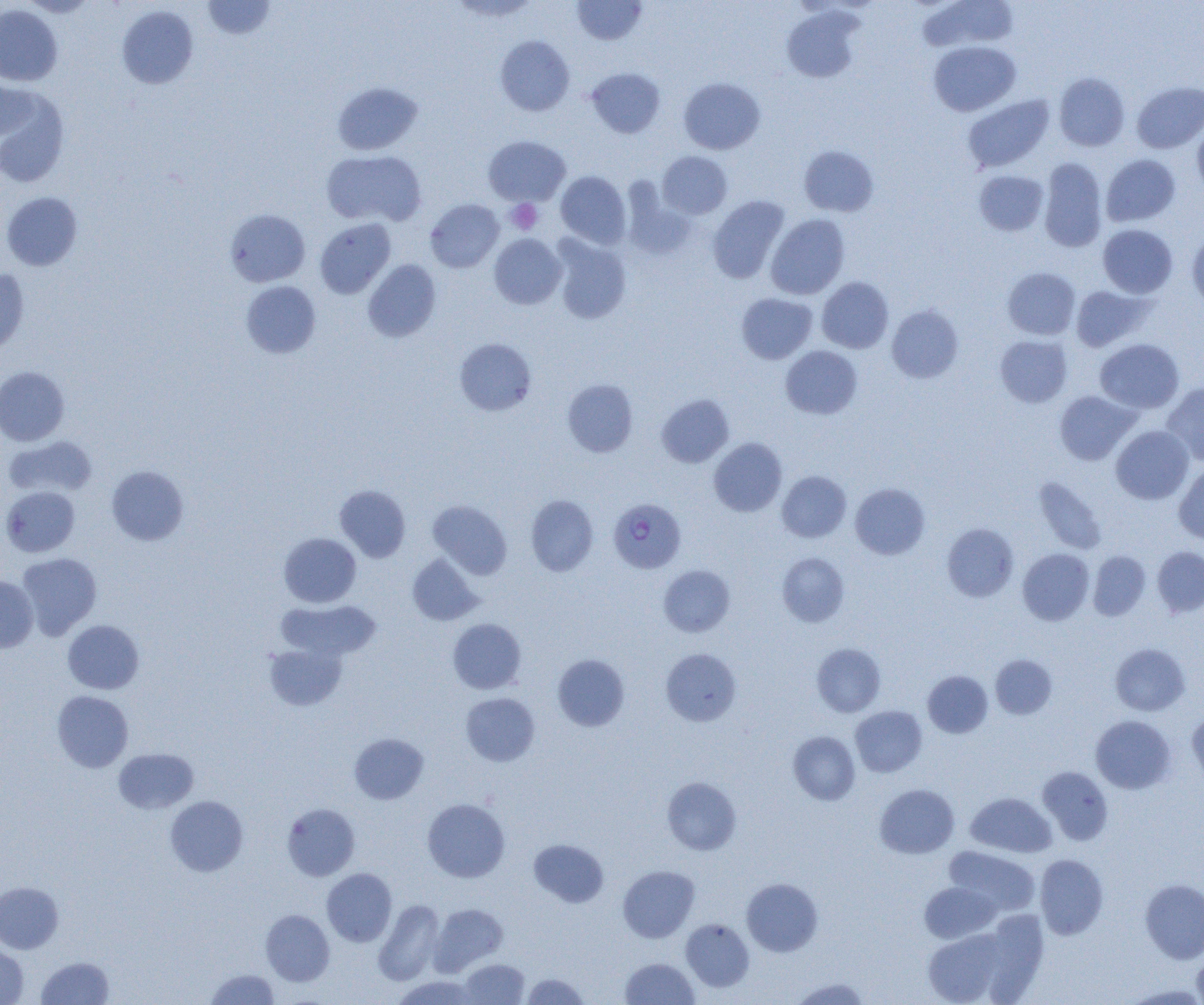 Approximate bounding boxes as named x1/y1/x2/y2 corners in pixels. Plasmodium falciparum-infected red blood cell locations: (x1=608, y1=497, x2=686, y2=573). Platelet locations: (x1=506, y1=199, x2=542, y2=234). Uninfected red blood cell locations: (x1=20, y1=0, x2=97, y2=17), (x1=203, y1=0, x2=275, y2=39), (x1=449, y1=0, x2=541, y2=21), (x1=572, y1=0, x2=647, y2=45), (x1=920, y1=0, x2=1017, y2=51), (x1=0, y1=5, x2=62, y2=86), (x1=117, y1=5, x2=198, y2=89), (x1=781, y1=6, x2=864, y2=83), (x1=495, y1=35, x2=575, y2=116), (x1=928, y1=41, x2=1020, y2=116), (x1=587, y1=67, x2=665, y2=138), (x1=1054, y1=73, x2=1130, y2=151), (x1=679, y1=77, x2=765, y2=154), (x1=0, y1=78, x2=38, y2=139), (x1=1132, y1=81, x2=1204, y2=153), (x1=332, y1=82, x2=423, y2=155), (x1=0, y1=89, x2=69, y2=187), (x1=962, y1=95, x2=1054, y2=172), (x1=1192, y1=121, x2=1204, y2=198), (x1=484, y1=136, x2=570, y2=206), (x1=799, y1=145, x2=879, y2=217), (x1=322, y1=150, x2=426, y2=227), (x1=657, y1=151, x2=732, y2=219), (x1=1101, y1=154, x2=1180, y2=227), (x1=1039, y1=158, x2=1108, y2=252), (x1=974, y1=170, x2=1048, y2=236), (x1=556, y1=171, x2=631, y2=249), (x1=622, y1=181, x2=696, y2=260), (x1=2, y1=192, x2=82, y2=271), (x1=708, y1=196, x2=790, y2=283), (x1=425, y1=199, x2=504, y2=272), (x1=225, y1=209, x2=310, y2=287), (x1=766, y1=214, x2=850, y2=299), (x1=314, y1=218, x2=396, y2=299), (x1=1098, y1=224, x2=1177, y2=298), (x1=1187, y1=231, x2=1204, y2=314), (x1=489, y1=234, x2=566, y2=309), (x1=550, y1=235, x2=631, y2=324), (x1=362, y1=259, x2=441, y2=342), (x1=1003, y1=267, x2=1080, y2=339), (x1=0, y1=268, x2=29, y2=355), (x1=817, y1=277, x2=893, y2=353), (x1=241, y1=281, x2=321, y2=358), (x1=1071, y1=285, x2=1152, y2=352), (x1=736, y1=293, x2=817, y2=363), (x1=887, y1=304, x2=964, y2=383), (x1=995, y1=335, x2=1072, y2=407), (x1=455, y1=338, x2=536, y2=416), (x1=1095, y1=338, x2=1184, y2=413), (x1=780, y1=346, x2=862, y2=419), (x1=0, y1=366, x2=69, y2=446), (x1=562, y1=379, x2=638, y2=457), (x1=1162, y1=382, x2=1204, y2=466), (x1=1055, y1=390, x2=1139, y2=465), (x1=657, y1=394, x2=734, y2=467), (x1=1111, y1=425, x2=1193, y2=504), (x1=3, y1=436, x2=97, y2=498), (x1=709, y1=438, x2=787, y2=517), (x1=1174, y1=463, x2=1204, y2=544), (x1=107, y1=465, x2=189, y2=545), (x1=777, y1=471, x2=851, y2=542), (x1=1033, y1=477, x2=1107, y2=555), (x1=851, y1=483, x2=930, y2=559), (x1=335, y1=485, x2=410, y2=562), (x1=1, y1=486, x2=80, y2=557), (x1=526, y1=495, x2=598, y2=576), (x1=428, y1=500, x2=512, y2=579), (x1=942, y1=523, x2=1019, y2=602), (x1=279, y1=532, x2=361, y2=607), (x1=1152, y1=546, x2=1204, y2=617), (x1=1018, y1=549, x2=1094, y2=625), (x1=1088, y1=550, x2=1150, y2=620), (x1=17, y1=553, x2=102, y2=639), (x1=777, y1=553, x2=849, y2=627), (x1=407, y1=554, x2=482, y2=625), (x1=658, y1=564, x2=735, y2=637), (x1=0, y1=575, x2=38, y2=654), (x1=276, y1=600, x2=381, y2=661), (x1=448, y1=618, x2=526, y2=694), (x1=63, y1=619, x2=144, y2=694), (x1=264, y1=643, x2=347, y2=710), (x1=812, y1=643, x2=885, y2=717), (x1=1110, y1=643, x2=1190, y2=716), (x1=661, y1=649, x2=741, y2=726), (x1=553, y1=654, x2=630, y2=731), (x1=990, y1=654, x2=1057, y2=719), (x1=923, y1=670, x2=993, y2=738), (x1=52, y1=691, x2=133, y2=772), (x1=461, y1=693, x2=540, y2=766), (x1=850, y1=706, x2=927, y2=777), (x1=1187, y1=713, x2=1204, y2=790), (x1=1091, y1=715, x2=1176, y2=793), (x1=788, y1=731, x2=860, y2=805), (x1=349, y1=733, x2=428, y2=804), (x1=114, y1=748, x2=199, y2=814), (x1=1037, y1=766, x2=1113, y2=845), (x1=662, y1=777, x2=741, y2=855), (x1=875, y1=784, x2=959, y2=858), (x1=966, y1=792, x2=1056, y2=857), (x1=165, y1=796, x2=248, y2=876), (x1=422, y1=798, x2=510, y2=882), (x1=282, y1=803, x2=360, y2=881), (x1=529, y1=839, x2=608, y2=907), (x1=944, y1=846, x2=1040, y2=915), (x1=1035, y1=854, x2=1108, y2=940), (x1=618, y1=865, x2=700, y2=942), (x1=322, y1=868, x2=397, y2=946), (x1=742, y1=878, x2=823, y2=956), (x1=1140, y1=878, x2=1204, y2=963), (x1=0, y1=881, x2=63, y2=954), (x1=920, y1=882, x2=1000, y2=943), (x1=374, y1=899, x2=444, y2=985), (x1=431, y1=904, x2=507, y2=973), (x1=261, y1=909, x2=334, y2=986), (x1=979, y1=912, x2=1048, y2=1002), (x1=681, y1=918, x2=754, y2=992), (x1=924, y1=929, x2=1007, y2=1004), (x1=0, y1=942, x2=28, y2=1004), (x1=1192, y1=950, x2=1204, y2=1005), (x1=36, y1=956, x2=114, y2=1004), (x1=621, y1=957, x2=699, y2=1005), (x1=460, y1=959, x2=530, y2=1004), (x1=205, y1=969, x2=280, y2=1004), (x1=522, y1=973, x2=590, y2=1004), (x1=392, y1=975, x2=480, y2=1005), (x1=789, y1=977, x2=871, y2=1004), (x1=1120, y1=983, x2=1204, y2=1004). Slide-level diagnosis: Plasmodium falciparum. Thin blood smear. Single field of view. Captured at 1000x magnification. Optical microscopy. Image is 1204×1005 pixels.